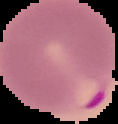
malaria status = parasitized
preparation = thin blood smear
image type = segmented cell region with the area outside set to black
image size = 118×124 pixels